Locate every Plasmodium parasite and every leukocyte.
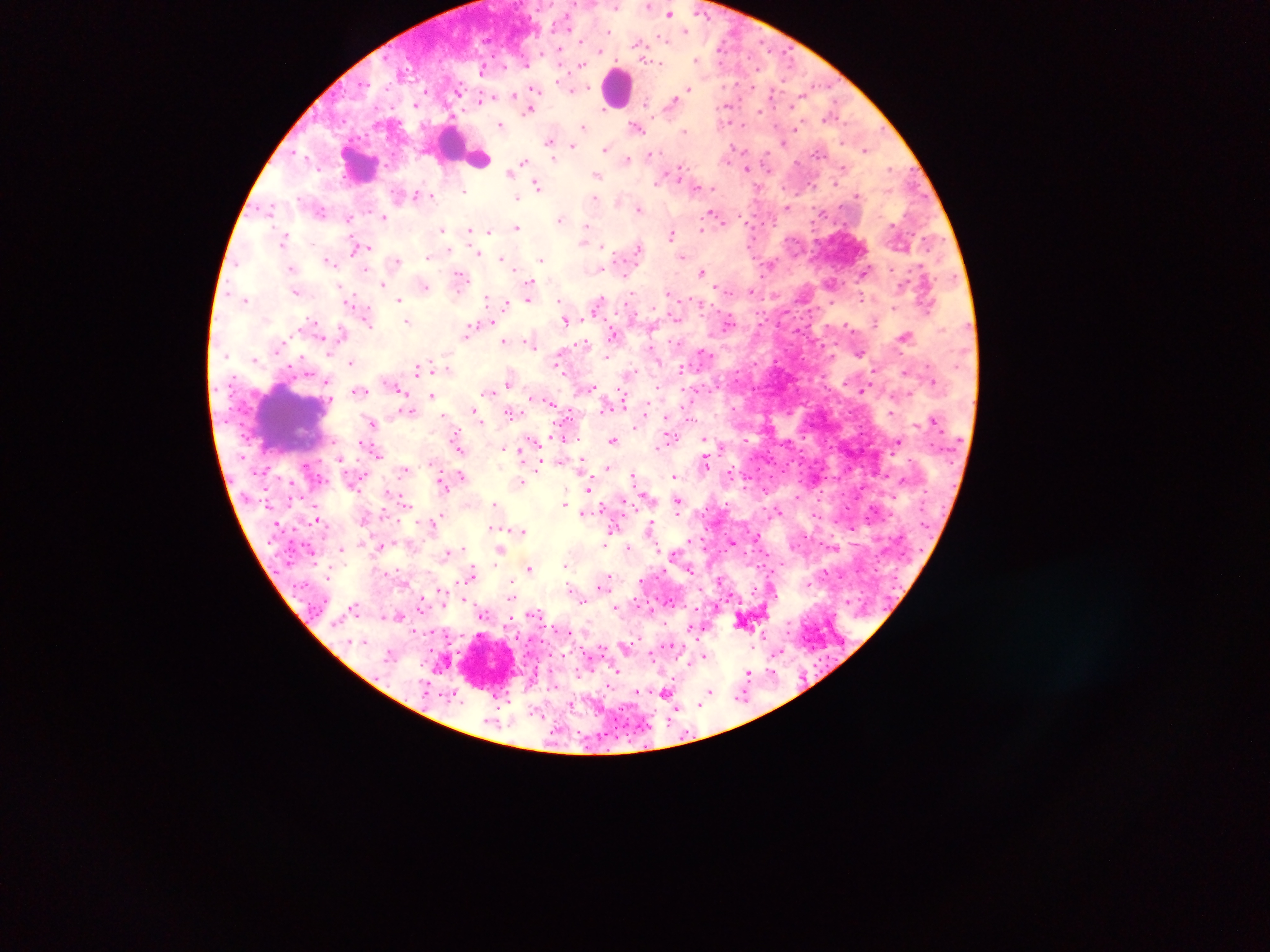
Approximate centers as {x, y} in pixels.
Plasmodium parasites: {616, 6}, {648, 6}, {671, 13}, {609, 31}, {666, 39}, {642, 44}, {697, 59}, {659, 62}, {580, 66}, {480, 69}, {537, 89}, {688, 89}, {575, 90}, {458, 93}, {512, 97}, {481, 99}, {417, 107}, {727, 108}, {530, 109}, {829, 117}, {502, 123}, {584, 126}, {640, 130}, {685, 130}, {783, 141}, {548, 142}, {572, 146}, {607, 148}, {866, 149}, {733, 151}, {650, 153}, {765, 157}, {629, 159}, {525, 161}, {747, 168}, {511, 170}, {892, 170}, {679, 171}, {750, 171}, {598, 176}, {536, 184}, {657, 184}, {463, 193}, {432, 194}, {415, 195}, {517, 198}, {596, 198}, {640, 208}, {788, 208}, {712, 212}, {348, 217}, {384, 217}, {561, 219}, {267, 223}, {723, 223}, {751, 223}, {517, 226}, {442, 229}, {470, 229}, {701, 229}, {489, 230}, {585, 233}, {671, 234}, {283, 239}, {365, 247}, {601, 248}, {354, 251}, {481, 252}, {684, 256}, {501, 257}, {542, 257}, {327, 258}, {429, 258}, {330, 261}, {398, 261}, {771, 264}, {289, 266}, {866, 271}, {702, 272}, {531, 280}, {833, 283}, {383, 286}, {426, 288}, {717, 289}, {752, 290}, {925, 293}, {774, 297}, {487, 299}, {527, 299}, {558, 299}, {865, 299}, {245, 300}, {400, 300}, {354, 301}, {505, 304}, {890, 308}, {566, 321}, {408, 322}, {727, 322}, {874, 323}, {369, 325}, {794, 330}, {467, 332}, {340, 334}, {504, 342}, {532, 346}, {859, 352}, {704, 354}, {608, 357}, {256, 358}, {351, 361}, {755, 362}, {431, 364}, {926, 368}, {417, 369}, {680, 369}, {560, 370}, {873, 370}, {328, 382}, {507, 383}, {796, 387}, {361, 391}, {863, 391}, {490, 392}, {404, 393}, {909, 394}, {431, 396}, {623, 399}, {549, 401}, {734, 407}, {472, 408}, {512, 414}, {891, 415}, {372, 423}, {456, 436}, {669, 436}, {613, 439}, {705, 439}, {563, 440}, {533, 441}, {897, 442}, {504, 446}, {829, 446}, {521, 447}, {377, 452}, {791, 460}, {707, 461}, {539, 464}, {267, 467}, {606, 467}, {633, 473}, {461, 474}, {744, 475}, {883, 475}, {675, 477}, {521, 480}, {441, 482}, {589, 487}, {649, 498}, {818, 501}, {564, 503}, {494, 504}, {678, 504}, {921, 508}, {869, 509}, {583, 510}, {777, 512}, {316, 518}, {650, 521}, {278, 526}, {650, 528}, {521, 530}, {757, 535}, {605, 540}, {733, 542}, {606, 544}, {379, 546}, {629, 546}, {837, 546}, {340, 548}, {500, 551}, {448, 553}, {565, 566}, {528, 568}, {823, 570}, {474, 571}, {857, 573}, {326, 578}, {508, 581}, {569, 587}, {439, 588}, {598, 588}, {511, 593}, {727, 599}, {465, 600}, {511, 600}, {670, 602}, {847, 602}, {420, 603}, {615, 606}, {353, 610}, {484, 615}, {399, 617}, {779, 654}, {699, 656}, {616, 672}, {749, 672}, {421, 680}, {709, 691}, {665, 693}, {638, 694}, {708, 696}, {741, 700}.
Leukocytes: {617, 93}, {455, 146}, {361, 162}, {291, 424}.

Image is 1270×952 pixels. Single field of view. Thick blood smear. Collected in Ghana. Photographed through a microscope with a mobile-phone camera.